Assess this cell for malaria.
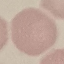

Uninfected.

preparation = thin blood film
capture = smartphone through the microscope eyepiece
stain = Giemsa
image type = automatically extracted cell patch, resized to 64 × 64 pixels